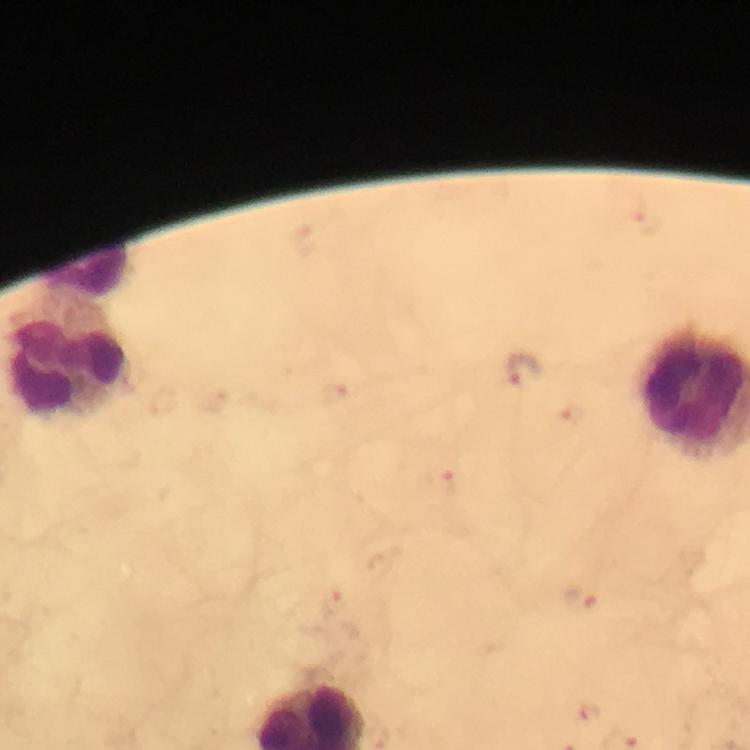
preparation = thick blood film
immersion oil = applied
capture = smartphone camera through the microscope
stain = Giemsa
cropped from = a single field of view
malaria parasite locations = approximate centers as [x, y] in pixels: [646, 221], [529, 368], [333, 395], [575, 419], [444, 483], [580, 600], [333, 601], [588, 712]
leukocyte locations = approximate centers as [x, y] in pixels: [84, 269], [69, 360]
context = from a diagnostic examination for malaria
image size = 750×750 pixels
magnification = 100x